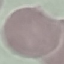

Summary:
  - Result: no malaria parasites seen
  - Preparation: thin blood smear
  - Stain: Giemsa
  - Image type: cell patch, automatically extracted from a larger field of view and resized to 64 × 64 pixels
  - Capture: smartphone camera at the microscope eyepiece